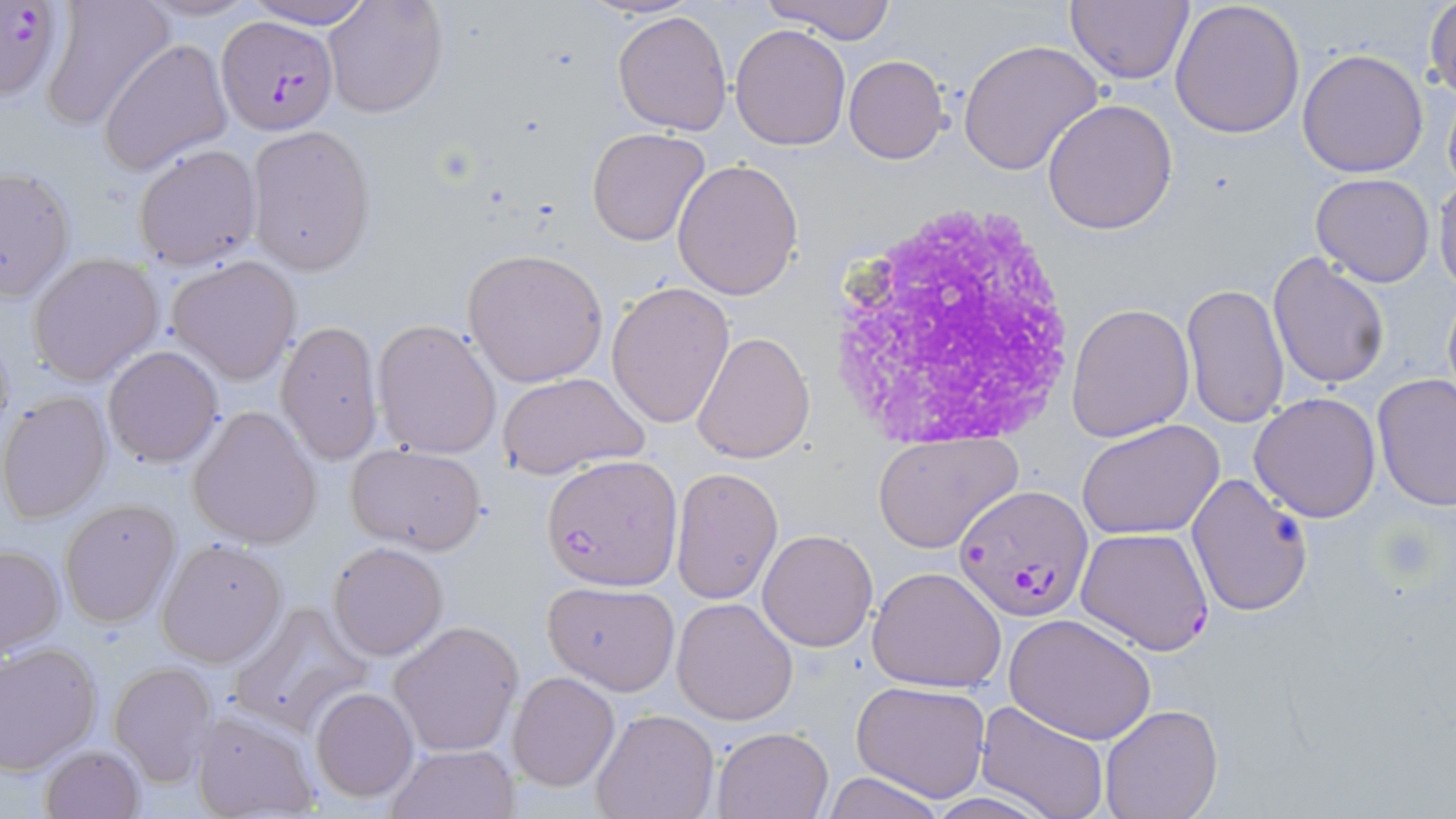
slide_level_diagnosis: Plasmodium falciparum
platelet_locations: 'approximate bounding boxes as (x1, y1, x2, y2) in pixels: (1379, 523, 1442, 586)'
magnification: 1000x
preparation: thin blood smear
white_blood_cell_locations: 'approximate bounding boxes as (x1, y1, x2, y2) in pixels: (823, 197, 1088, 450)'
field_of_view: one of a larger specimen
uninfected_red_blood_cell_locations: 'approximate bounding boxes as (x1, y1, x2, y2) in pixels: (39, 0, 175, 132), (131, 0, 262, 24), (244, 0, 375, 28), (322, 0, 448, 120), (761, 0, 897, 43), (1067, 0, 1194, 86), (1170, 0, 1306, 139), (1427, 0, 1456, 102), (612, 9, 734, 135), (731, 24, 851, 150), (100, 38, 232, 177), (958, 39, 1103, 178), (1297, 48, 1429, 177), (844, 55, 948, 164), (1441, 75, 1456, 198), (1044, 97, 1178, 234), (245, 123, 377, 274), (586, 126, 711, 246), (133, 143, 262, 270), (672, 160, 804, 302), (0, 164, 77, 304), (1309, 173, 1436, 285), (1432, 176, 1456, 295), (462, 248, 608, 386), (1267, 252, 1391, 389), (27, 253, 164, 385), (166, 256, 302, 385), (606, 281, 735, 429), (1181, 283, 1291, 429), (1068, 303, 1193, 442), (275, 318, 385, 466), (372, 318, 503, 461), (693, 331, 816, 466), (102, 345, 223, 467), (496, 372, 648, 477), (1373, 373, 1456, 510), (1, 391, 115, 524), (1249, 391, 1382, 522), (188, 405, 323, 548), (1077, 420, 1224, 540), (874, 434, 1021, 553), (347, 444, 487, 555), (670, 466, 784, 604), (1187, 471, 1313, 618), (58, 498, 181, 629), (757, 530, 877, 652), (156, 539, 287, 668), (327, 542, 450, 661), (0, 544, 64, 657), (867, 566, 1006, 693), (542, 580, 681, 695), (671, 597, 799, 723), (228, 602, 373, 735), (1005, 614, 1155, 744), (390, 621, 524, 757), (0, 642, 101, 773), (109, 662, 216, 785), (507, 672, 620, 792), (850, 680, 991, 803), (309, 686, 419, 803), (974, 701, 1111, 819), (1099, 704, 1222, 819), (188, 707, 321, 819), (591, 709, 718, 819), (713, 725, 835, 818), (39, 744, 144, 819), (386, 745, 517, 819), (823, 771, 946, 819)'
image_size: 1456×819 pixels
plasmodium_falciparum_infected_red_blood_cell_locations: 'approximate bounding boxes as (x1, y1, x2, y2) in pixels: (0, 0, 67, 101), (216, 15, 340, 137), (542, 456, 682, 590), (956, 484, 1090, 620), (1076, 527, 1215, 654)'
stain: May-Grünwald-Giemsa
modality: optical microscopy